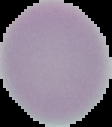
{
  "malaria_status": "uninfected",
  "image_size": "112×127 pixels",
  "preparation": "thin blood film",
  "image_type": "segmented cell region on a black background"
}